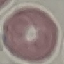

Summary:
  - Result: negative for malaria parasites
  - Capture: smartphone through the microscope eyepiece
  - Preparation: thin blood smear
  - Image type: automatically extracted cell patch, resized to 64 × 64 pixels
  - Stain: Giemsa